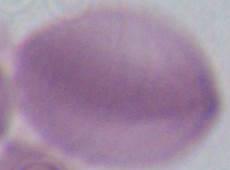
1000x magnification. An erythrocyte is shown. Micrograph.